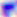
Summary:
  - Identification: Toxoplasma gondii
  - Magnification: 400x
  - Modality: micrograph